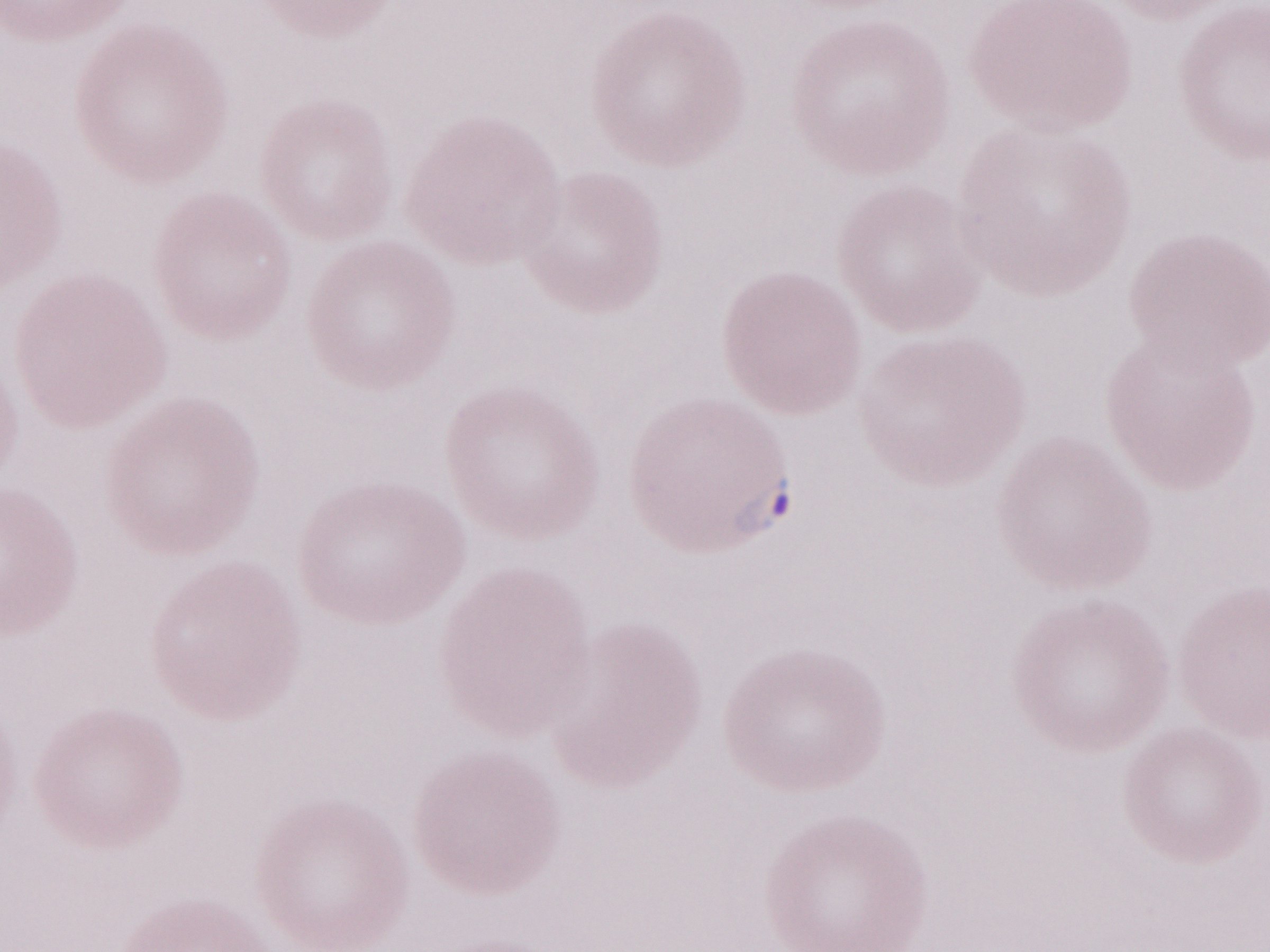
Image is 1270×952 pixels. May-Grünwald-Giemsa (MGG) stain. Olympus BX43 microscope and DP73 digital camera. One field of this slide. Thin blood film. Patient diagnosis: malaria infection. 1,000x magnification.